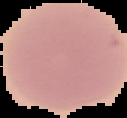
Summary:
  - Result: negative for malaria parasites
  - Image type: segmented cell region on a black background
  - Preparation: thin blood film
  - Image size: 127×118 pixels